Identify the parasite.
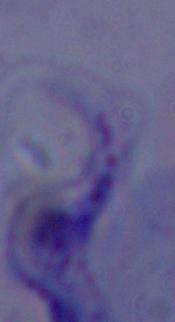

This is a trypanosome.

Summary:
  - Magnification: 1000x
  - Modality: photomicrograph